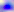

Captured at 400x magnification. Toxoplasma gondii is shown. Micrograph.